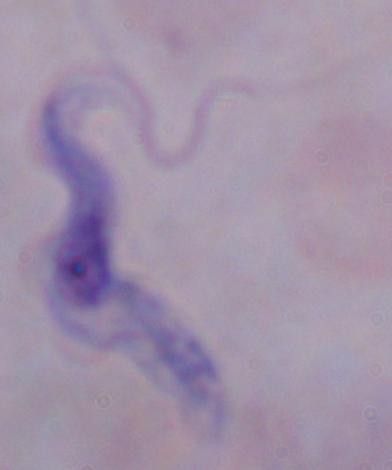
Summary:
  - Magnification: 1000x
  - Modality: photomicrograph
  - Identification: trypanosome